Outline each Plasmodium vivax-infected red blood cell.
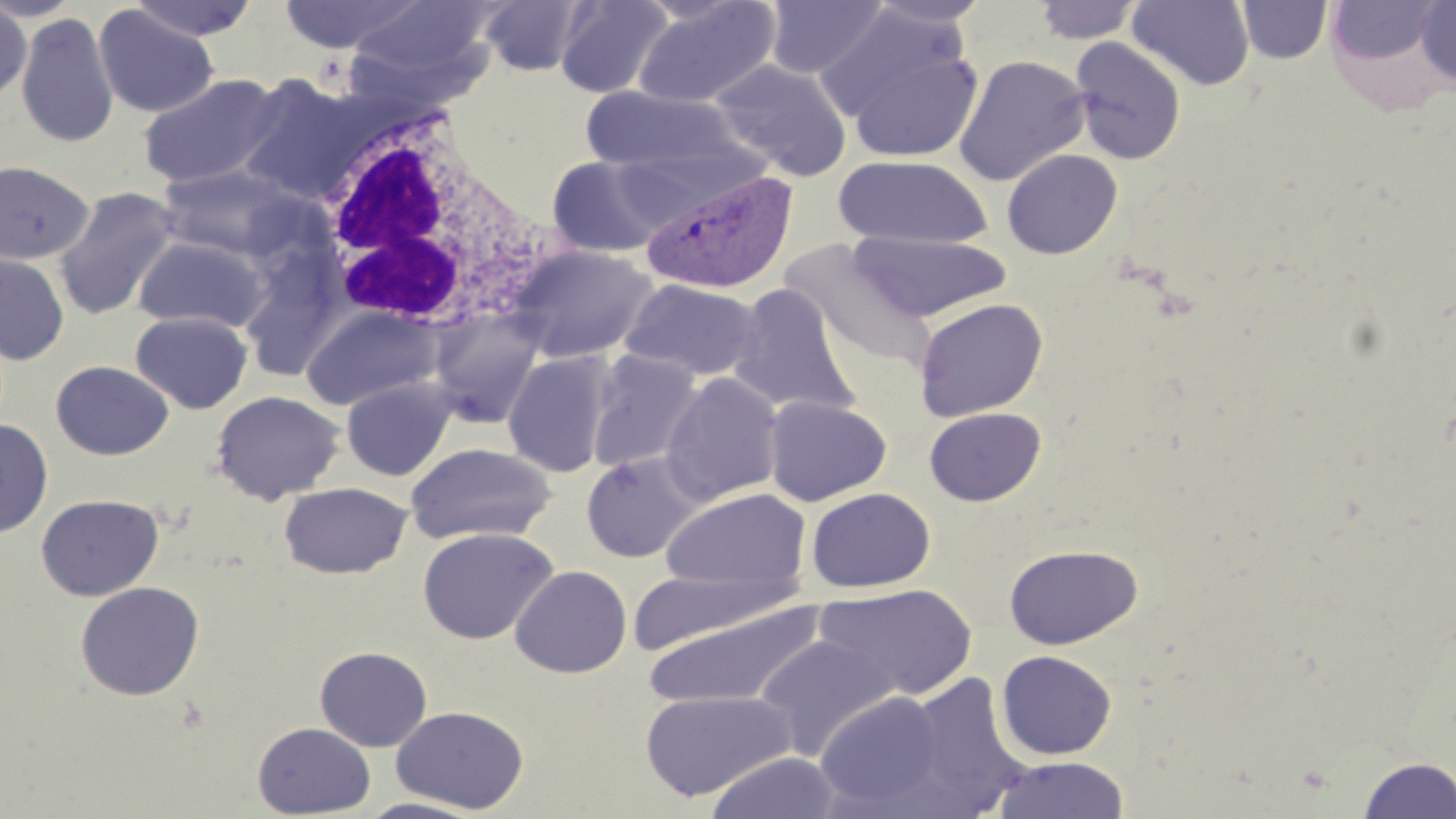
Approximate bounding boxes as (x1,y1)-(x2,y2) corner pairs in pixels.
Plasmodium vivax-infected red blood cells: (640,166)-(800,296).

Uninfected red blood cell locations: (0,0)-(84,22), (129,0)-(260,41), (278,0)-(423,54), (478,0)-(590,76), (554,0)-(674,98), (863,0)-(993,29), (1126,0)-(1255,90), (631,1)-(783,109), (763,1)-(888,79), (1032,1)-(1144,44), (1236,1)-(1332,64), (1414,1)-(1456,87), (0,2)-(32,102), (1328,2)-(1444,71), (343,3)-(496,93), (817,4)-(966,123), (93,5)-(218,118), (15,13)-(119,147), (1069,36)-(1186,165), (842,45)-(984,164), (953,54)-(1090,186), (710,59)-(851,180), (238,71)-(370,204), (139,73)-(285,189), (579,86)-(754,176), (1001,149)-(1122,259), (546,155)-(671,257), (834,155)-(993,249), (0,160)-(94,266), (156,163)-(301,259), (53,185)-(181,320), (849,231)-(1012,323), (132,235)-(270,332), (780,241)-(935,369), (508,244)-(657,363), (0,253)-(69,365), (621,278)-(762,382), (728,282)-(860,418), (913,297)-(1049,420), (302,305)-(443,411), (427,309)-(547,428), (130,311)-(252,414), (586,350)-(702,472), (502,351)-(616,477), (51,360)-(174,460), (660,372)-(784,506), (341,377)-(456,481), (211,390)-(345,505), (764,396)-(892,506), (924,406)-(1046,506), (0,419)-(53,537), (405,443)-(556,546), (580,451)-(704,563), (279,482)-(412,579), (662,487)-(811,592), (806,488)-(936,593), (35,493)-(164,601), (417,527)-(558,645), (1004,544)-(1143,649), (510,565)-(632,678), (630,571)-(810,655), (75,581)-(205,701), (815,583)-(979,700), (640,599)-(826,709), (753,633)-(903,761), (315,646)-(432,751), (996,650)-(1117,760), (900,672)-(1030,816), (639,689)-(797,801), (815,690)-(947,811), (391,706)-(529,814), (252,722)-(376,818), (703,751)-(844,818), (1357,754)-(1456,819), (989,756)-(1131,818), (356,797)-(489,818). White blood cell locations: (310,112)-(550,336). Slide-level diagnosis: Plasmodium vivax. May-Grünwald-Giemsa stain. 1000x magnification. Optical microscopy. Image is 1456×819 pixels. Single field of view. Thin blood film.